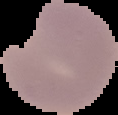

From a thin blood film. Image is 118×115 pixels. Malaria status: parasitized. The area outside the segmented cell region is set to black.